Outline each uninfected red blood cell.
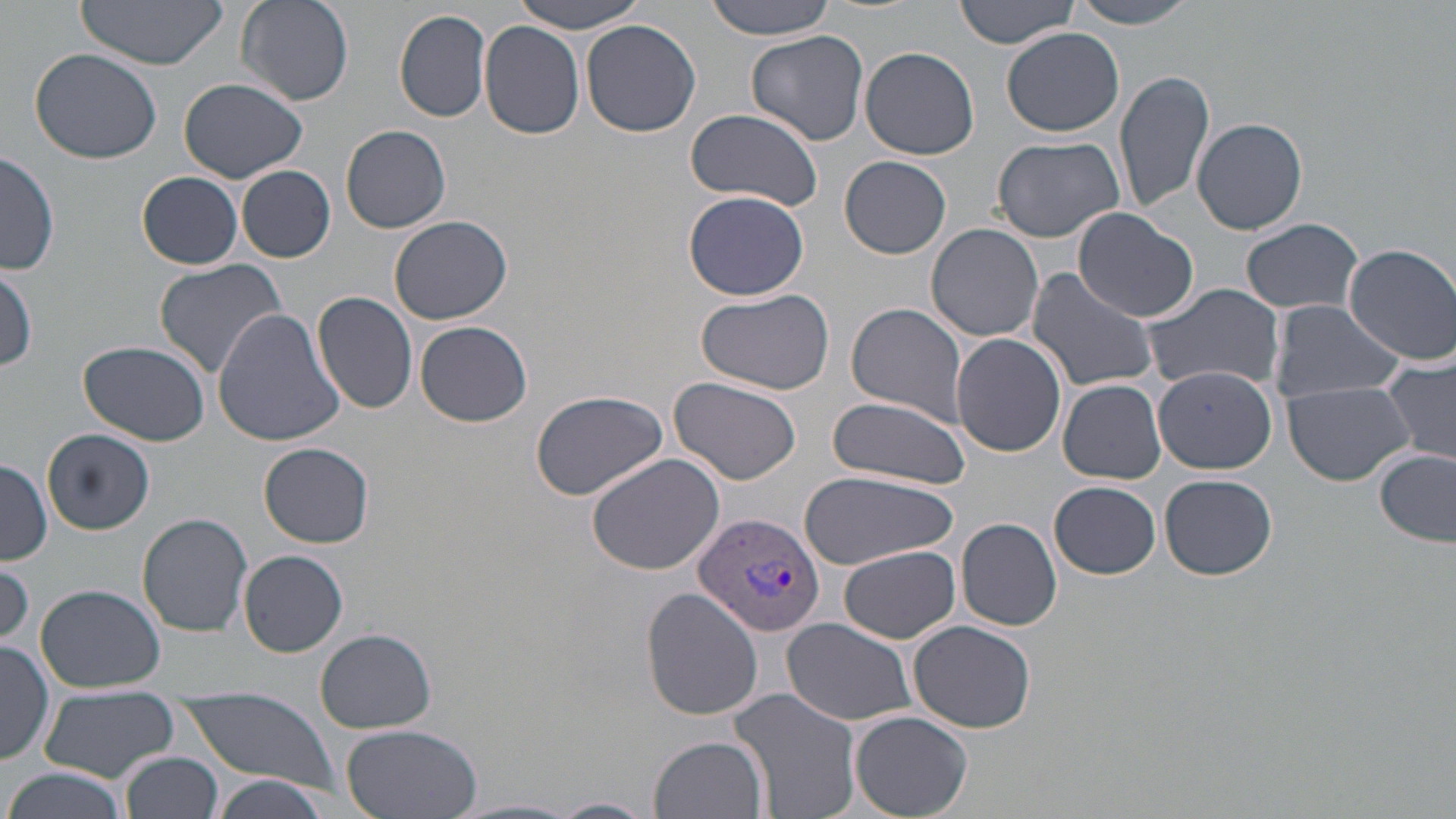

Approximate bounding boxes as (x1,y1)-(x2,y2) corner pairs in pixels.
Uninfected red blood cells: (74,0)-(231,68), (236,0)-(354,108), (507,0)-(655,33), (704,0)-(840,39), (954,0)-(1080,49), (1073,0)-(1203,28), (395,9)-(492,124), (580,19)-(702,137), (480,22)-(586,139), (1002,28)-(1127,136), (747,30)-(870,148), (30,47)-(163,165), (861,47)-(981,161), (1114,67)-(1215,218), (180,77)-(307,183), (685,108)-(823,209), (1191,118)-(1307,235), (342,125)-(451,233), (991,135)-(1126,242), (1,150)-(60,276), (840,156)-(951,258), (237,166)-(335,263), (136,170)-(244,269), (684,190)-(809,301), (1071,209)-(1199,322), (388,213)-(512,324), (1241,219)-(1364,314), (927,224)-(1045,343), (1344,242)-(1456,364), (152,258)-(290,380), (0,265)-(39,372), (1026,269)-(1158,393), (1141,282)-(1285,395), (695,288)-(836,398), (313,290)-(420,415), (1268,299)-(1404,405), (846,301)-(968,426), (212,309)-(345,447), (413,320)-(534,426), (952,335)-(1067,459), (79,341)-(211,447), (1380,356)-(1456,469), (1152,365)-(1278,473), (670,376)-(807,489), (1059,379)-(1167,484), (1284,379)-(1414,486), (531,391)-(668,501), (825,395)-(973,490), (43,429)-(154,535), (261,441)-(374,547), (1374,448)-(1455,546), (586,452)-(727,576), (0,456)-(51,565), (799,471)-(958,569), (1159,472)-(1277,580), (1050,480)-(1160,577), (137,513)-(254,635), (956,518)-(1061,631), (840,546)-(960,642), (238,549)-(349,657), (1,559)-(33,646), (35,582)-(166,693), (642,588)-(765,720), (781,618)-(918,726), (909,620)-(1036,733), (314,627)-(439,734), (0,640)-(53,767), (39,687)-(180,781), (730,687)-(862,819), (177,689)-(340,789), (850,710)-(972,819), (336,723)-(485,819), (650,734)-(768,819), (121,751)-(223,819), (4,766)-(127,819), (211,775)-(331,819), (550,797)-(657,819), (453,799)-(584,819).

Plasmodium vivax-infected red blood cell locations: (693,511)-(826,639). Slide-level diagnosis: Plasmodium vivax. Image is 1456×819 pixels. One field of a larger specimen. May-Grünwald-Giemsa stain. Captured at 1000x magnification. Thin blood smear. Light microscopy.